Report the malaria status of this cell.
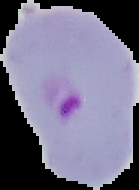

It is parasitized.

image type = cell region segmented out of the field of view; surrounding area masked to black
preparation = thin blood smear
image size = 139×190 pixels